Locate platelets.
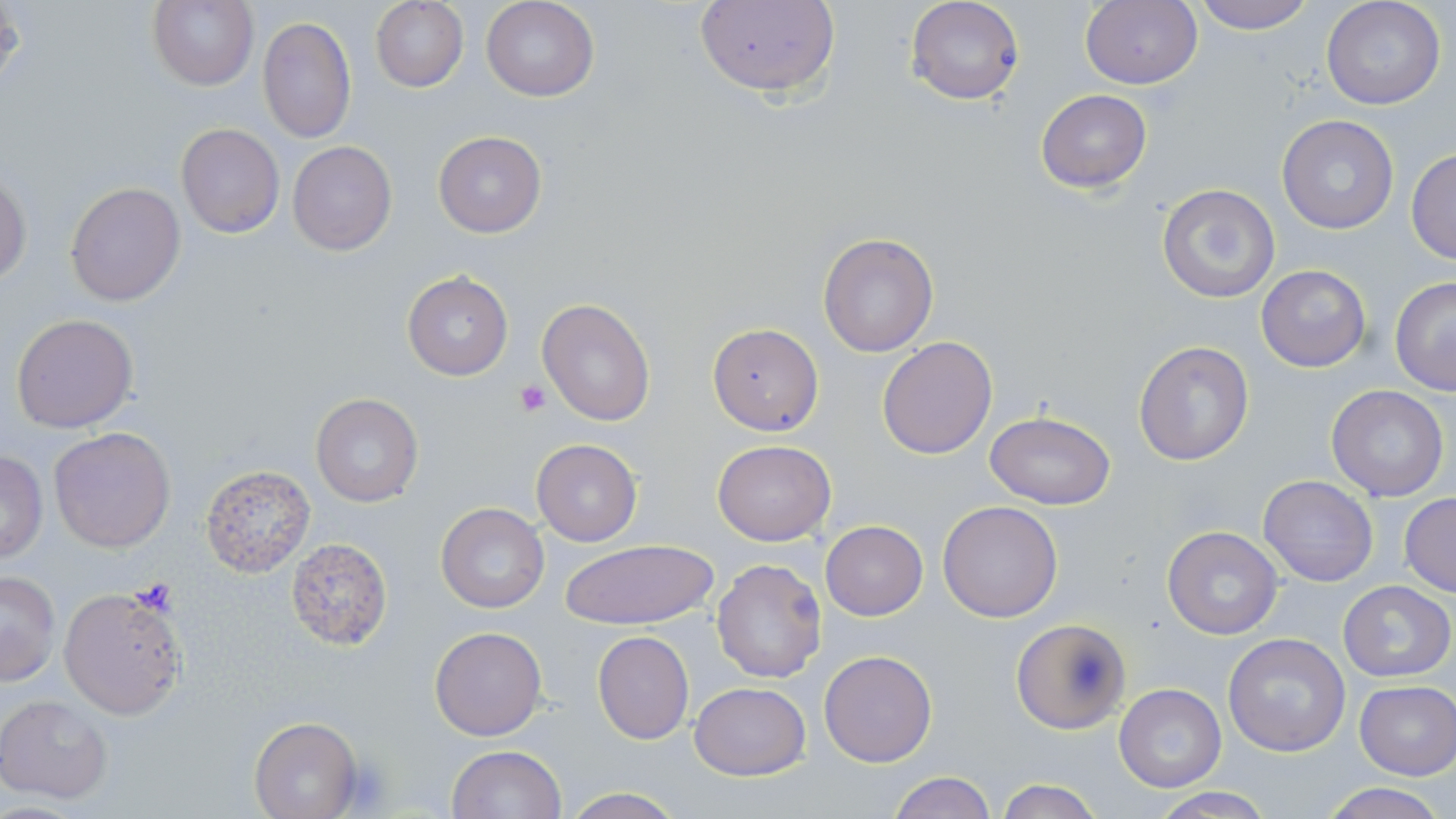

Approximate bounding boxes as (x1,y1)-(x2,y2) corner pairs in pixels.
Platelets: (515,378)-(550,415), (130,579)-(181,617), (339,755)-(398,813).

Uninfected red blood cell locations: (148,0)-(258,90), (481,0)-(599,102), (692,0)-(841,100), (905,0)-(1025,106), (1080,0)-(1201,91), (1190,0)-(1315,34), (1321,0)-(1446,111), (369,1)-(469,91), (257,16)-(356,142), (1037,89)-(1151,192), (1277,114)-(1400,235), (176,122)-(284,238), (433,131)-(547,237), (288,141)-(397,255), (1406,148)-(1456,264), (0,170)-(31,289), (66,182)-(186,306), (1157,183)-(1279,303), (818,232)-(939,357), (1256,264)-(1371,372), (402,272)-(513,381), (1390,276)-(1456,394), (538,299)-(655,427), (10,313)-(139,432), (706,322)-(824,436), (878,336)-(998,458), (1133,340)-(1255,467), (1326,384)-(1450,501), (310,392)-(423,508), (985,411)-(1116,510), (48,426)-(177,552), (531,438)-(642,547), (711,438)-(836,547), (1,449)-(48,563), (198,464)-(317,577), (1258,474)-(1378,587), (1400,493)-(1456,596), (938,499)-(1064,621), (436,502)-(550,613), (821,520)-(927,619), (1162,526)-(1285,639), (287,537)-(393,649), (559,540)-(718,631), (712,558)-(828,684), (1,569)-(61,686), (1338,581)-(1454,682), (58,586)-(187,719), (1011,618)-(1131,733), (430,626)-(547,741), (591,631)-(693,744), (1222,633)-(1349,757), (819,648)-(937,767), (1354,681)-(1455,780), (690,682)-(810,781), (1114,684)-(1226,794), (1,693)-(117,805), (249,717)-(361,819), (445,746)-(566,819), (887,772)-(997,819), (994,778)-(1103,819), (1316,782)-(1449,819), (561,787)-(684,819), (1146,789)-(1277,818). Slide-level diagnosis: Plasmodium falciparum. Single field of view. Optical microscopy. May-Grünwald-Giemsa stain. Thin blood film. 1000x magnification. Image is 1456×819 pixels.